Locate and identify every blood parasite.
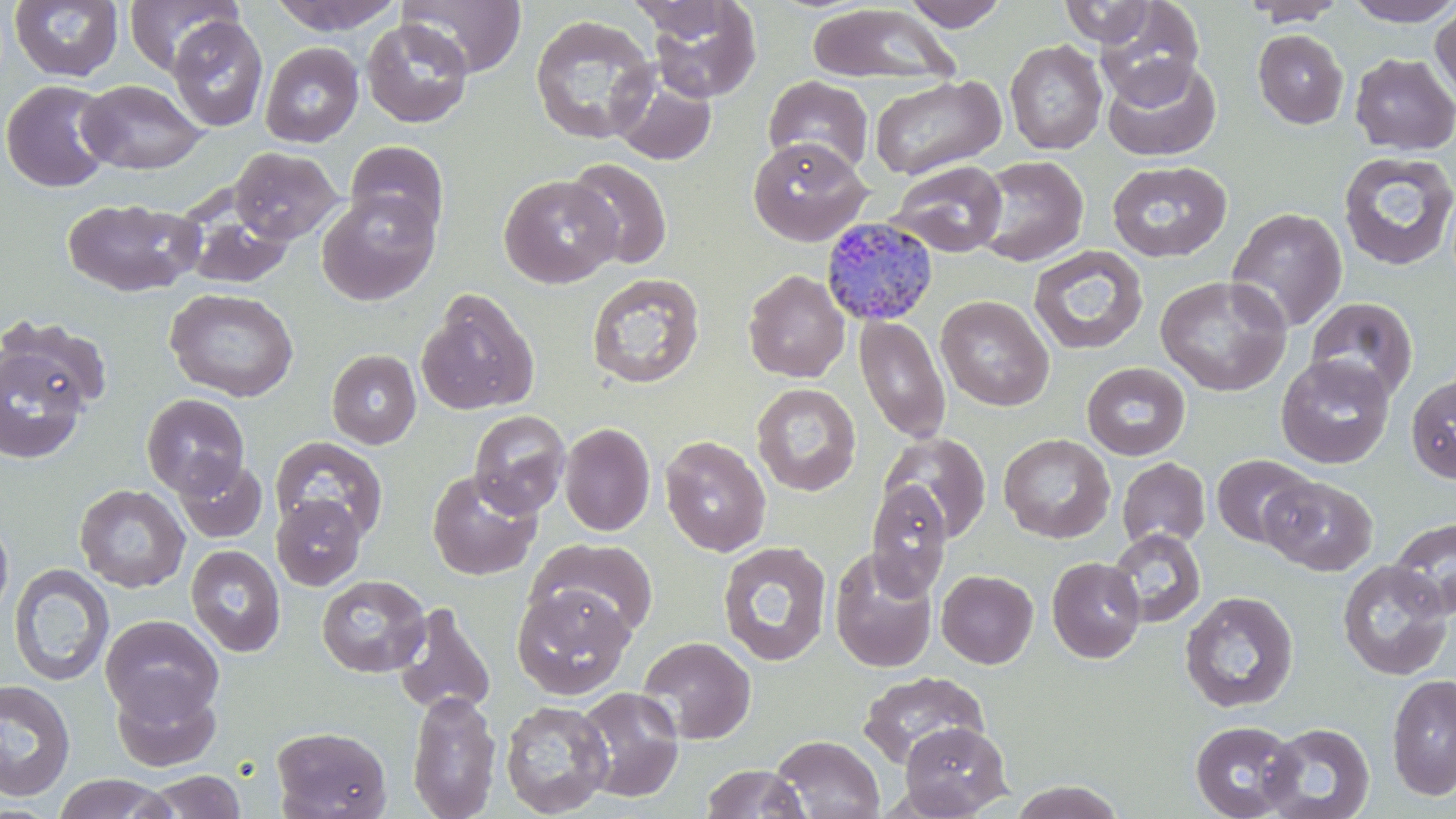
Approximate bounding boxes as (x1,y1)-(x2,y2) corner pairs in pixels.
Plasmodium malariae-infected red blood cells: (819,217)-(940,327).
No Plasmodium falciparum, Plasmodium ovale, Plasmodium vivax, Babesia divergens, or Trypanosoma brucei observed.

Uninfected red blood cell locations: (123,0)-(242,75), (269,0)-(404,35), (398,0)-(527,78), (901,0)-(1008,30), (1095,0)-(1204,106), (1242,0)-(1345,26), (1342,0)-(1456,27), (9,1)-(124,82), (643,1)-(762,103), (1058,1)-(1158,47), (807,4)-(961,86), (1430,4)-(1456,108), (529,14)-(658,145), (168,16)-(268,132), (362,18)-(473,128), (1253,28)-(1349,129), (1005,40)-(1108,155), (260,42)-(364,147), (1350,52)-(1456,155), (1103,58)-(1221,161), (610,69)-(717,167), (763,75)-(874,176), (869,75)-(1005,180), (1,79)-(116,192), (76,80)-(208,175), (747,136)-(871,246), (345,140)-(449,239), (229,147)-(342,245), (1337,150)-(1456,271), (972,155)-(1089,267), (565,157)-(672,270), (888,160)-(1008,258), (1107,160)-(1232,262), (499,174)-(621,287), (317,191)-(439,306), (63,197)-(203,298), (180,204)-(295,289), (1225,206)-(1347,334), (1027,245)-(1149,356), (743,269)-(850,383), (586,273)-(705,389), (1155,275)-(1291,396), (165,288)-(300,402), (417,288)-(540,416), (936,295)-(1054,412), (1305,296)-(1418,402), (854,314)-(951,444), (2,315)-(113,415), (0,341)-(91,465), (326,349)-(421,449), (1276,354)-(1395,469), (1081,362)-(1191,460), (1406,373)-(1456,484), (751,383)-(861,496), (141,393)-(250,498), (468,410)-(571,518), (559,422)-(656,536), (879,432)-(992,543), (998,433)-(1115,543), (271,435)-(389,542), (659,435)-(771,557), (1211,454)-(1316,548), (173,456)-(268,543), (1116,457)-(1211,550), (427,468)-(542,580), (1260,476)-(1378,575), (866,481)-(952,599), (74,484)-(190,593), (271,494)-(367,590), (0,512)-(14,625), (1389,516)-(1456,620), (1107,528)-(1206,627), (528,538)-(658,639), (717,541)-(832,667), (185,545)-(286,657), (829,548)-(938,672), (1046,556)-(1146,663), (1336,560)-(1454,681), (8,563)-(115,686), (936,570)-(1038,668), (316,574)-(430,677), (512,584)-(634,700), (1180,590)-(1298,714), (390,601)-(496,718), (100,615)-(224,723), (637,636)-(756,744), (858,670)-(988,768), (1386,673)-(1456,800), (110,677)-(222,772), (1,679)-(76,801), (574,686)-(686,803), (406,690)-(502,819), (500,699)-(613,817), (1189,719)-(1302,819), (898,721)-(1013,817), (1260,722)-(1375,819), (271,726)-(392,819), (771,735)-(885,818), (700,763)-(810,819), (144,770)-(247,818), (52,774)-(176,818), (1008,780)-(1125,818). Slide-level diagnosis: Plasmodium malariae. Captured at 1000x magnification. Image is 1456×819 pixels. One field of a larger specimen. Thin blood smear. May-Grünwald-Giemsa-stained preparation. Light microscopy.